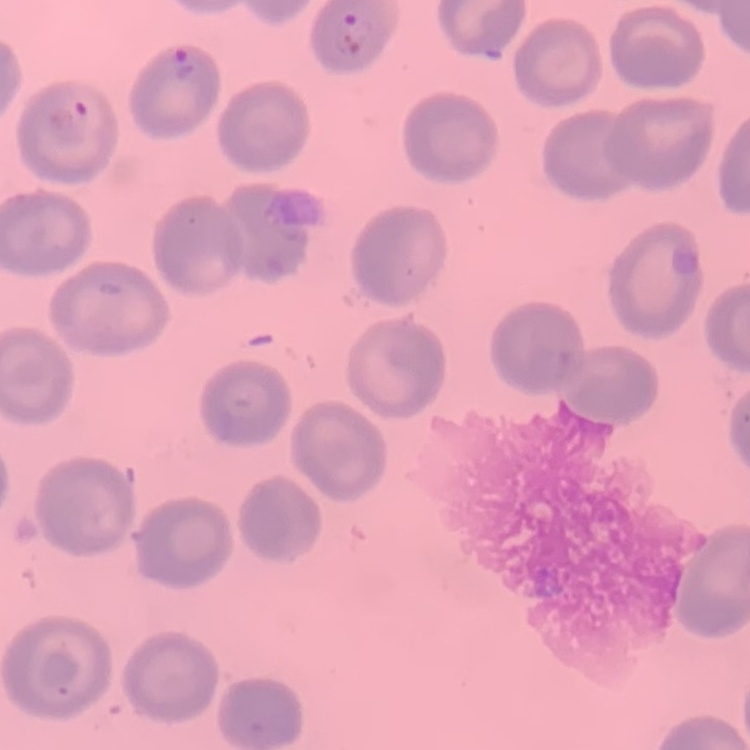
Summary:
  - Red blood cell morphology: no rouleaux formation
  - Stain: Field's or Giemsa
  - Image type: one tile cut from a larger photomicrograph
  - Preparation: thin blood film